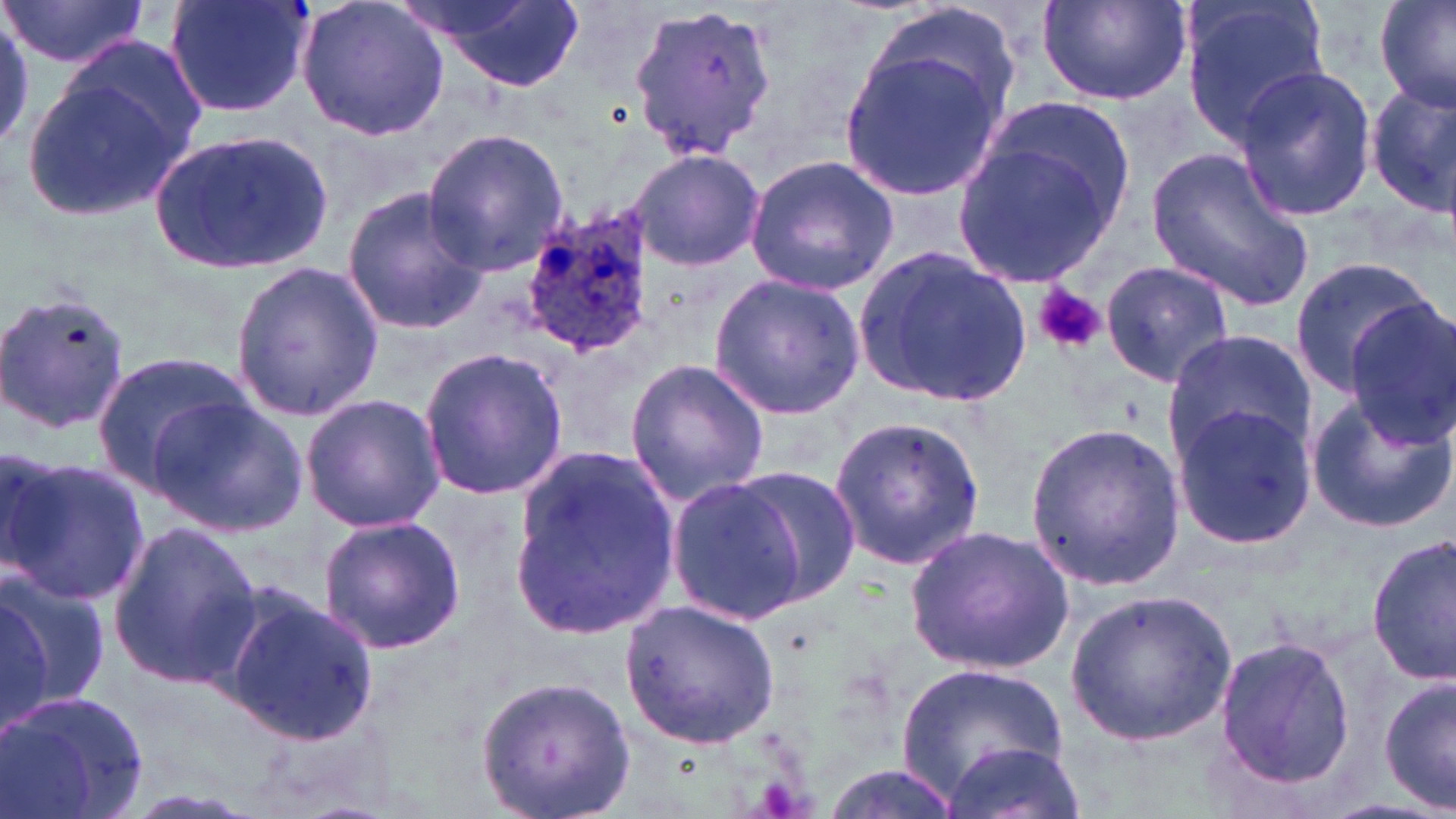
slide_level_diagnosis: Plasmodium ovale
modality: light microscopy
magnification: 1000x
platelet_locations: 'approximate bounding boxes as (x1,y1)-(x2,y2) corner pairs in pixels: (1034,286)-(1105,353)'
field_of_view: single
preparation: thin blood film
image_size: 1456×819 pixels
stain: May-Grünwald-Giemsa
uninfected_red_blood_cell_locations: 'approximate bounding boxes as (x1,y1)-(x2,y2) corner pairs in pixels: (2,0)-(155,67), (165,0)-(315,121), (297,0)-(450,142), (411,0)-(585,91), (1180,0)-(1333,150), (1375,0)-(1456,114), (1037,1)-(1191,106), (625,3)-(776,160), (0,10)-(34,150), (837,39)-(1013,201), (26,54)-(201,222), (1228,64)-(1379,222), (1365,84)-(1456,214), (148,125)-(337,275), (422,129)-(570,275), (952,133)-(1123,289), (1147,147)-(1315,312), (629,148)-(766,272), (744,156)-(898,296), (341,186)-(490,333), (855,246)-(1030,408), (1288,256)-(1437,394), (228,259)-(384,420), (1100,260)-(1235,389), (708,274)-(867,420), (0,288)-(133,437), (1345,304)-(1455,447), (1163,328)-(1316,463), (416,346)-(568,502), (89,351)-(259,493), (624,357)-(771,507), (1304,391)-(1455,535), (301,393)-(447,533), (152,397)-(308,537), (1169,405)-(1318,547), (826,412)-(985,576), (1025,422)-(1184,590), (510,443)-(684,639), (3,456)-(150,608), (727,465)-(862,603), (665,474)-(813,625), (316,514)-(465,655), (109,521)-(262,688), (905,522)-(1077,676), (1368,532)-(1456,684), (0,566)-(111,709), (0,585)-(50,736), (216,587)-(382,746), (1065,590)-(1237,748), (621,598)-(781,749), (1211,634)-(1355,793), (900,661)-(1066,794), (475,676)-(634,818), (1380,676)-(1455,814), (0,688)-(151,819), (940,742)-(1088,819), (817,765)-(962,818)'
plasmodium_ovale_infected_red_blood_cell_locations: 'approximate bounding boxes as (x1,y1)-(x2,y2) corner pairs in pixels: (516,206)-(656,360)'